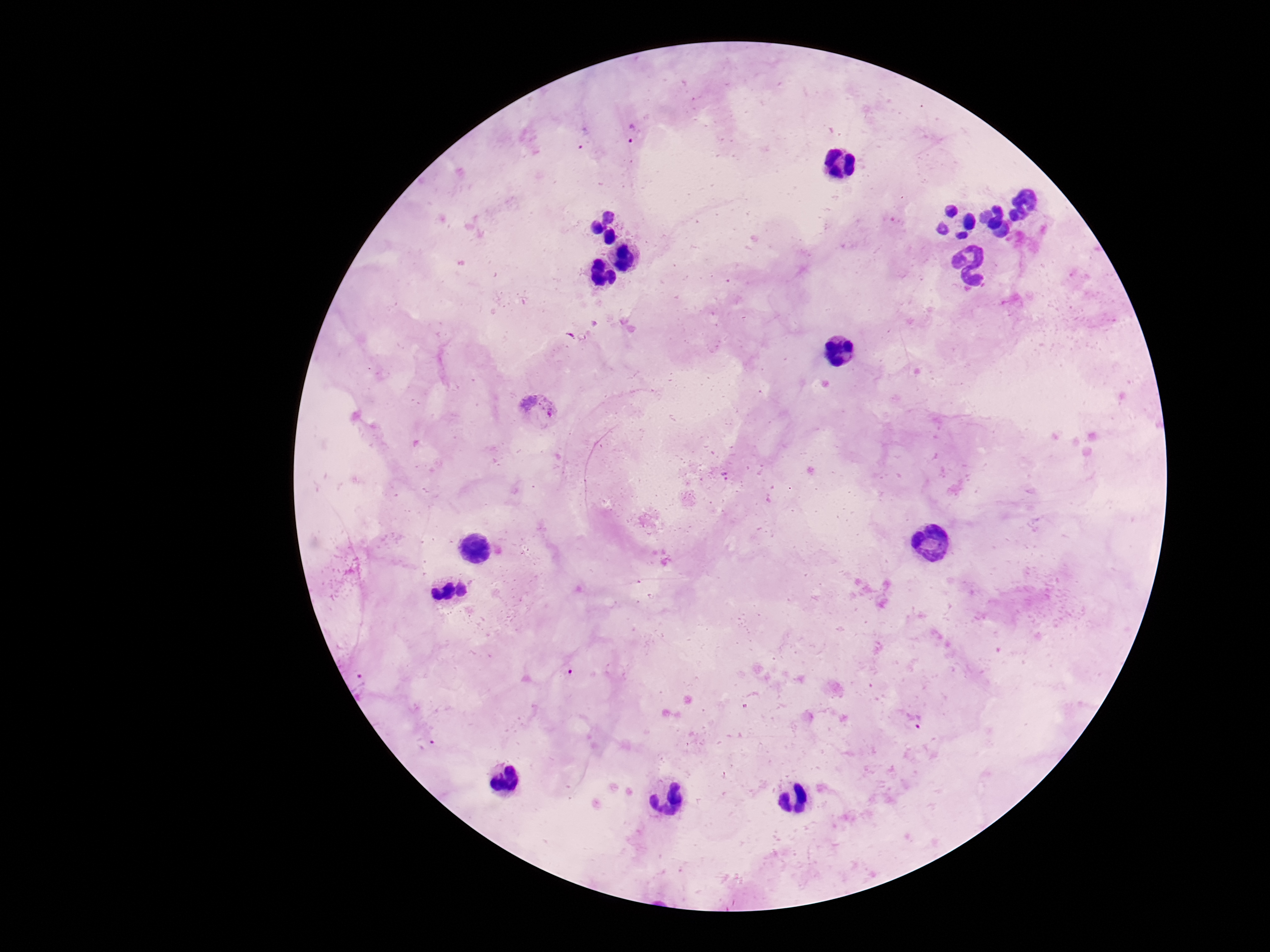

Approximate object centers, in pixels from the top-left corner. Plasmodium parasite locations: (x=631, y=135), (x=539, y=410), (x=725, y=475), (x=359, y=681), (x=915, y=721), (x=425, y=743). 100x magnification. Single field of view. Photographed through the microscope eyepiece with a smartphone camera. Patient malaria status: positive. Thick blood smear. Image is 1270×952 pixels. Giemsa-stained preparation.